Classify this cell by malaria status.
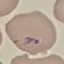
It is parasitized.

preparation: thin blood smear
image_type: cell patch, automatically extracted from a larger field of view and resized to 64 × 64 pixels
capture: smartphone through the microscope eyepiece
stain: Giemsa